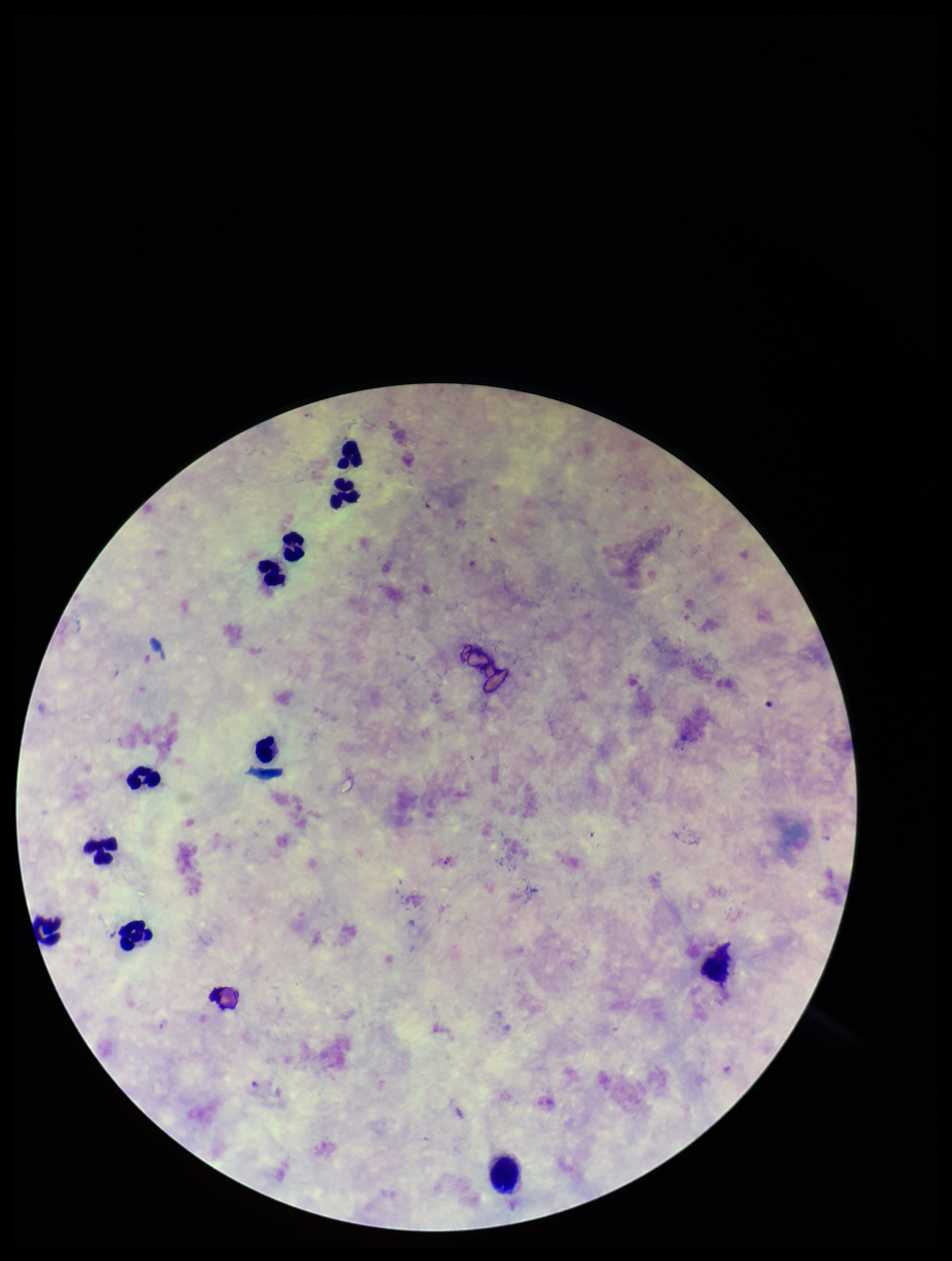

preparation = thick smear
patient malaria status = infected
capture = smartphone photograph through the microscope eyepiece
Plasmodium parasites = none identified
species reported for this patient = Plasmodium falciparum
stain = Giemsa
image size = 952×1261 pixels
field of view = single
leukocyte count = 11
parasite count = 0